Give the extent of all uninfected red blood cells.
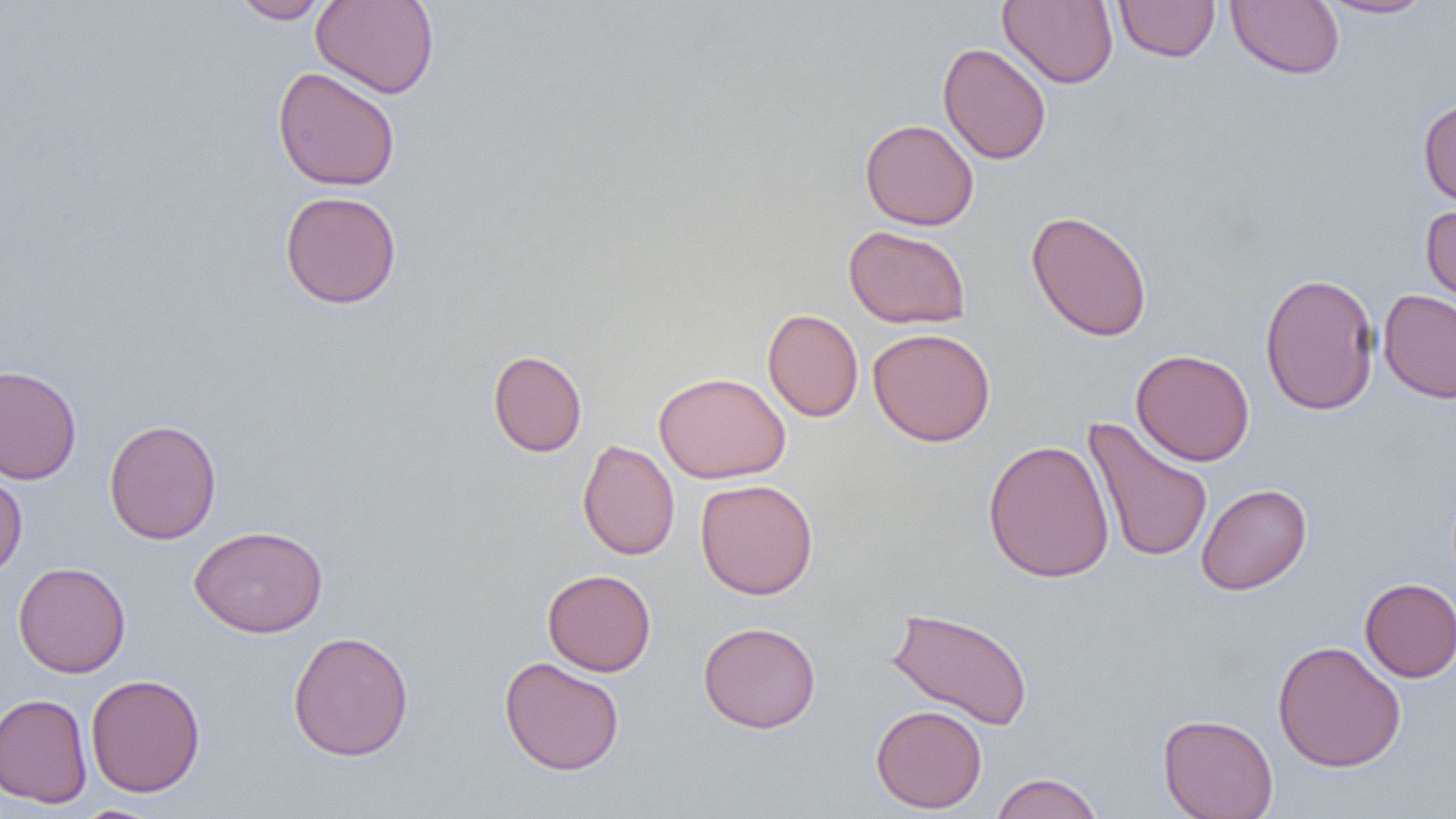

Approximate bounding boxes as (x1, y1, x2, y2) in pixels.
Uninfected red blood cells: (231, 0, 331, 23), (311, 0, 440, 99), (998, 0, 1118, 89), (1316, 0, 1434, 19), (1114, 1, 1220, 62), (1226, 1, 1345, 79), (937, 43, 1052, 164), (272, 66, 400, 192), (1418, 98, 1456, 209), (860, 118, 979, 230), (279, 190, 402, 309), (1420, 203, 1456, 315), (1025, 209, 1152, 342), (843, 224, 971, 329), (1259, 272, 1379, 416), (1378, 289, 1456, 404), (762, 308, 863, 422), (867, 327, 995, 447), (487, 349, 587, 457), (1131, 349, 1255, 466), (0, 364, 82, 485), (653, 372, 791, 483), (1082, 417, 1213, 563), (104, 419, 222, 545), (577, 439, 680, 561), (983, 439, 1115, 583), (0, 468, 27, 581), (695, 479, 818, 599), (1196, 483, 1311, 595), (189, 524, 328, 638), (13, 561, 131, 678), (542, 569, 656, 676), (1359, 578, 1456, 682), (885, 606, 1034, 730), (698, 621, 822, 734), (287, 630, 414, 761), (1271, 640, 1407, 772), (499, 656, 625, 775), (85, 674, 206, 797), (0, 693, 93, 808), (870, 705, 987, 813), (1158, 713, 1278, 819), (989, 772, 1104, 819), (71, 805, 166, 819).

Summary:
  - Slide-level diagnosis: no evidence of blood parasites
  - Field of view: one of a larger specimen
  - Modality: light microscopy
  - Preparation: thin blood smear
  - Magnification: 1000x
  - Image size: 1456×819 pixels